Assess the morphology of the erythrocytes.
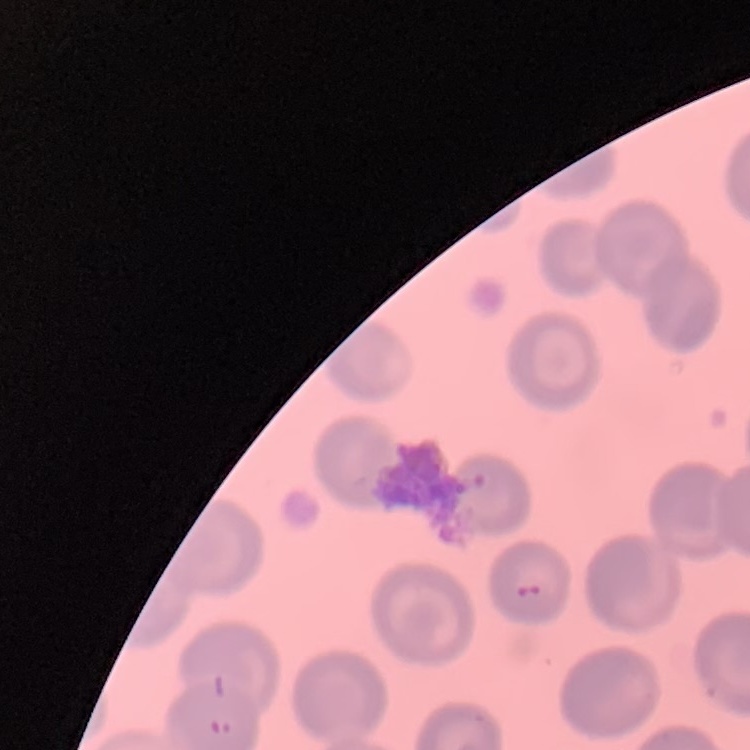
No rouleaux formation.

image type = square crop of a larger photomicrograph
stain = Field's or Giemsa
preparation = thin peripheral smear